Comment on the morphology of the erythrocytes.
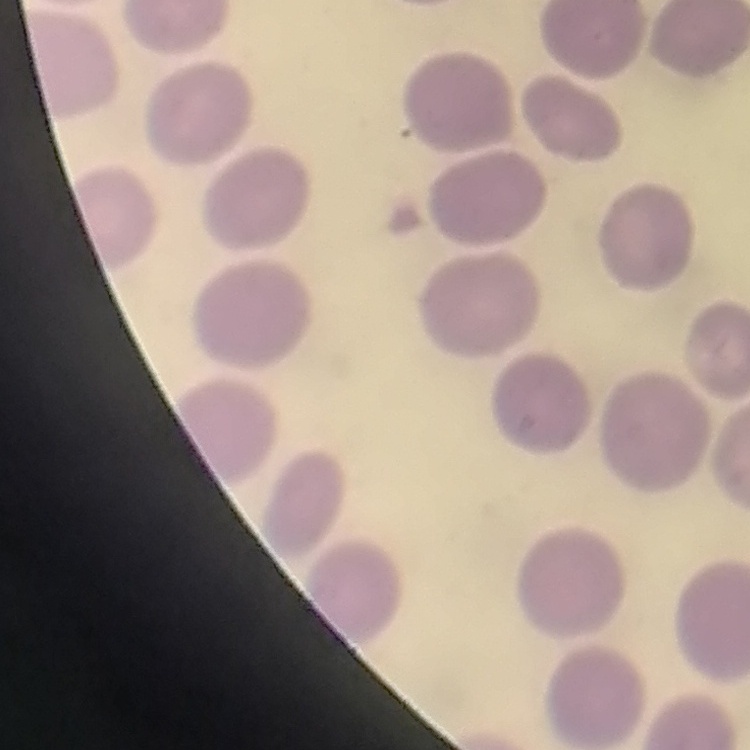

They show no rouleaux formation.

Summary:
  - Stain: Field's or Giemsa
  - Preparation: thin peripheral smear
  - Image type: square crop of a larger photomicrograph